Classify this cell by malaria status.
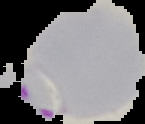

It is parasitized.

Summary:
  - Image size: 145×124 pixels
  - Preparation: thin blood smear
  - Image type: cell region segmented out of the field of view; surrounding area masked to black